Describe the morphology of the red blood cells.
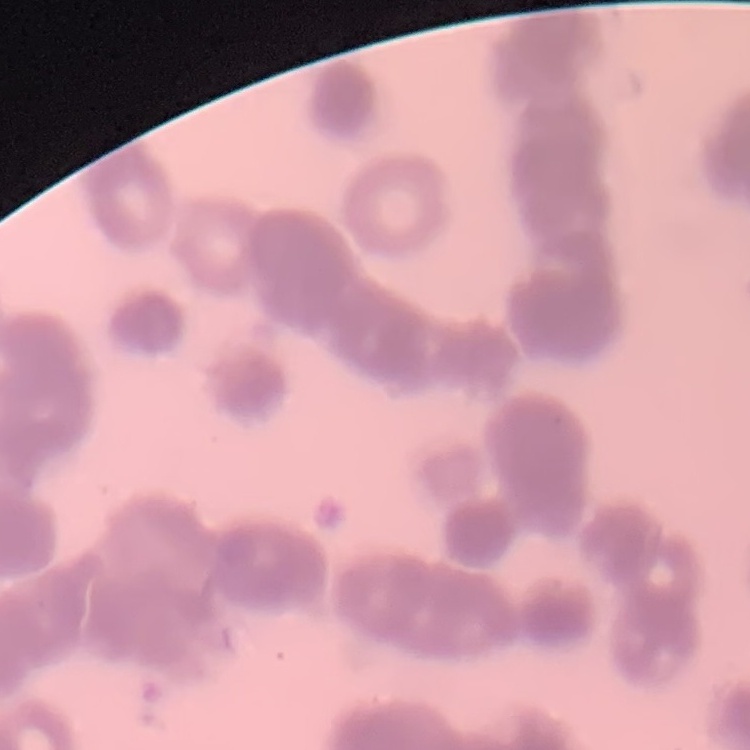
They show rouleaux formation.

Thin peripheral smear. Field's or Giemsa stain. Square crop of a larger photomicrograph.